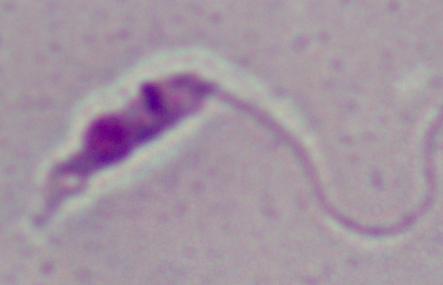
Summary:
  - Modality: micrograph
  - Identification: Leishmania
  - Magnification: 1000x